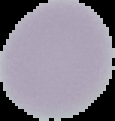

image type = segmented cell region with the area outside set to black
malaria status = uninfected
image size = 115×121 pixels
preparation = thin blood film